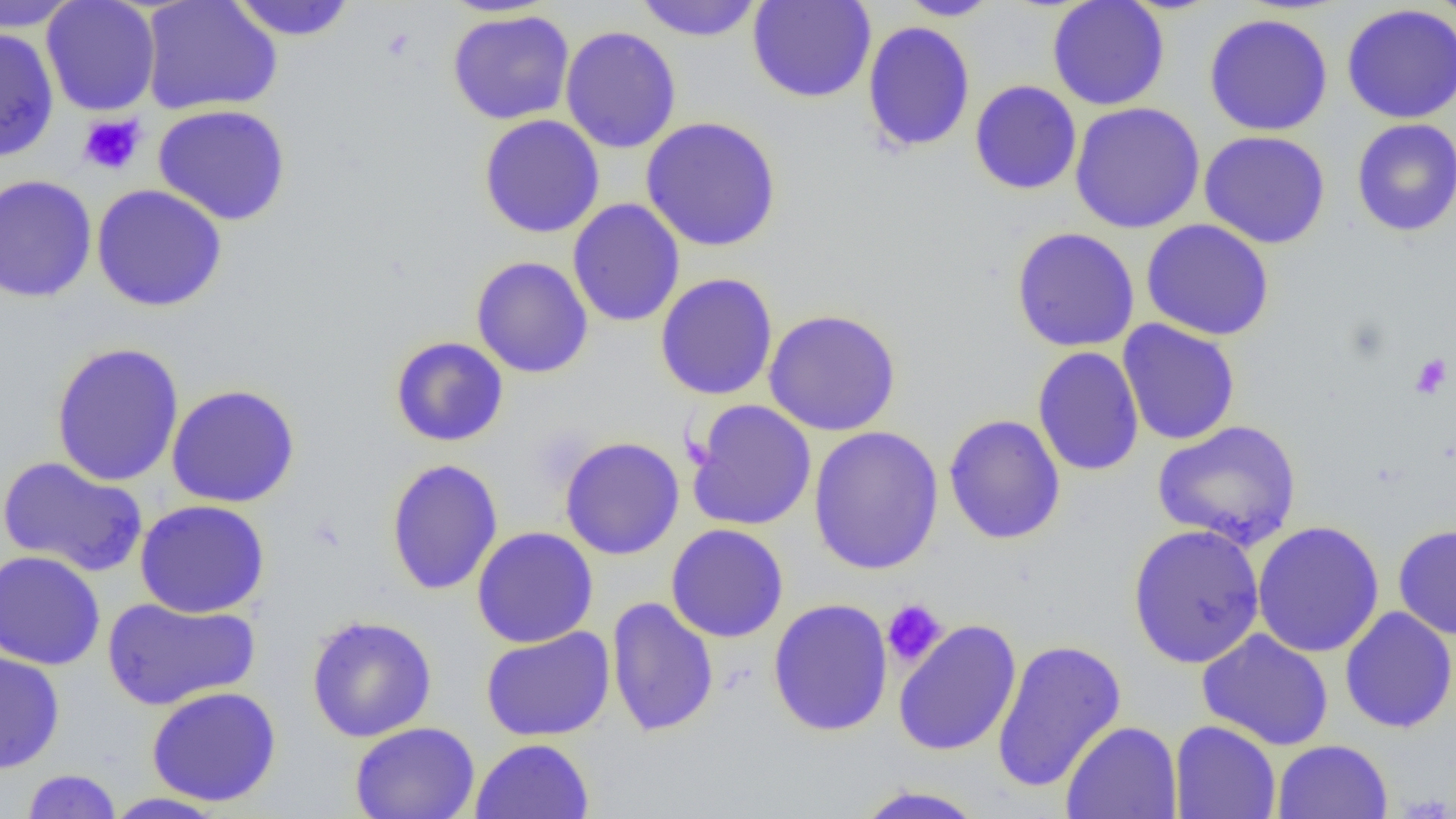
Summary:
  - Coordinate format: approximate bounding boxes as named x1/y1/x2/y2 corners in pixels
  - Uninfected red blood cell locations: (x1=0, y1=0, x2=80, y2=31), (x1=41, y1=0, x2=161, y2=116), (x1=140, y1=0, x2=282, y2=116), (x1=634, y1=0, x2=764, y2=42), (x1=747, y1=0, x2=877, y2=103), (x1=897, y1=0, x2=1003, y2=20), (x1=1047, y1=0, x2=1170, y2=111), (x1=1431, y1=0, x2=1456, y2=33), (x1=227, y1=1, x2=358, y2=41), (x1=1341, y1=4, x2=1456, y2=124), (x1=447, y1=10, x2=575, y2=125), (x1=1203, y1=13, x2=1333, y2=136), (x1=862, y1=20, x2=975, y2=154), (x1=560, y1=25, x2=682, y2=154), (x1=0, y1=28, x2=59, y2=163), (x1=969, y1=79, x2=1082, y2=195), (x1=1069, y1=102, x2=1205, y2=233), (x1=152, y1=104, x2=292, y2=226), (x1=478, y1=114, x2=606, y2=239), (x1=640, y1=116, x2=782, y2=252), (x1=1351, y1=118, x2=1456, y2=237), (x1=1199, y1=130, x2=1331, y2=249), (x1=0, y1=175, x2=98, y2=302), (x1=91, y1=183, x2=228, y2=312), (x1=568, y1=198, x2=685, y2=328), (x1=1141, y1=219, x2=1275, y2=341), (x1=1011, y1=226, x2=1141, y2=352), (x1=470, y1=256, x2=593, y2=379), (x1=654, y1=272, x2=779, y2=401), (x1=763, y1=307, x2=902, y2=437), (x1=1117, y1=319, x2=1241, y2=446), (x1=390, y1=336, x2=509, y2=447), (x1=50, y1=341, x2=185, y2=487), (x1=1032, y1=346, x2=1144, y2=477), (x1=166, y1=383, x2=301, y2=508), (x1=686, y1=399, x2=817, y2=531), (x1=943, y1=414, x2=1066, y2=545), (x1=1151, y1=420, x2=1303, y2=551), (x1=807, y1=425, x2=945, y2=576), (x1=559, y1=436, x2=685, y2=560), (x1=1, y1=455, x2=149, y2=578), (x1=385, y1=458, x2=504, y2=595), (x1=134, y1=499, x2=271, y2=618), (x1=1251, y1=520, x2=1385, y2=658), (x1=1127, y1=523, x2=1266, y2=669), (x1=1393, y1=523, x2=1456, y2=639), (x1=666, y1=524, x2=789, y2=643), (x1=471, y1=526, x2=599, y2=648), (x1=1, y1=550, x2=106, y2=670), (x1=101, y1=596, x2=260, y2=711), (x1=606, y1=596, x2=719, y2=738), (x1=767, y1=598, x2=894, y2=737), (x1=1339, y1=606, x2=1456, y2=733), (x1=306, y1=614, x2=437, y2=742), (x1=893, y1=619, x2=1022, y2=756), (x1=480, y1=626, x2=616, y2=741), (x1=1196, y1=629, x2=1334, y2=751), (x1=992, y1=639, x2=1127, y2=793), (x1=0, y1=651, x2=65, y2=773), (x1=146, y1=686, x2=282, y2=807), (x1=1169, y1=720, x2=1281, y2=819), (x1=1061, y1=721, x2=1182, y2=819), (x1=349, y1=722, x2=481, y2=819), (x1=470, y1=738, x2=594, y2=819), (x1=1272, y1=739, x2=1392, y2=819), (x1=20, y1=768, x2=122, y2=818), (x1=851, y1=784, x2=989, y2=819), (x1=102, y1=792, x2=230, y2=818)
  - Platelet locations: (x1=78, y1=113, x2=146, y2=176), (x1=1409, y1=353, x2=1452, y2=399), (x1=882, y1=599, x2=948, y2=669)
  - Slide-level diagnosis: no evidence of blood parasites
  - Modality: optical microscopy
  - Preparation: thin blood smear
  - Field of view: single
  - Magnification: 1000x
  - Image size: 1456×819 pixels